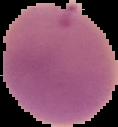
preparation = thin blood film
image size = 118×127 pixels
image type = cell region segmented out of the field of view; surrounding area masked to black
result = malaria parasites detected